Classify this cell by malaria status.
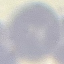
It is uninfected.

Summary:
  - Preparation: thin blood film
  - Stain: Giemsa
  - Image type: cell patch, automatically extracted from a larger field of view and resized to 64 × 64 pixels
  - Capture: smartphone through the microscope eyepiece